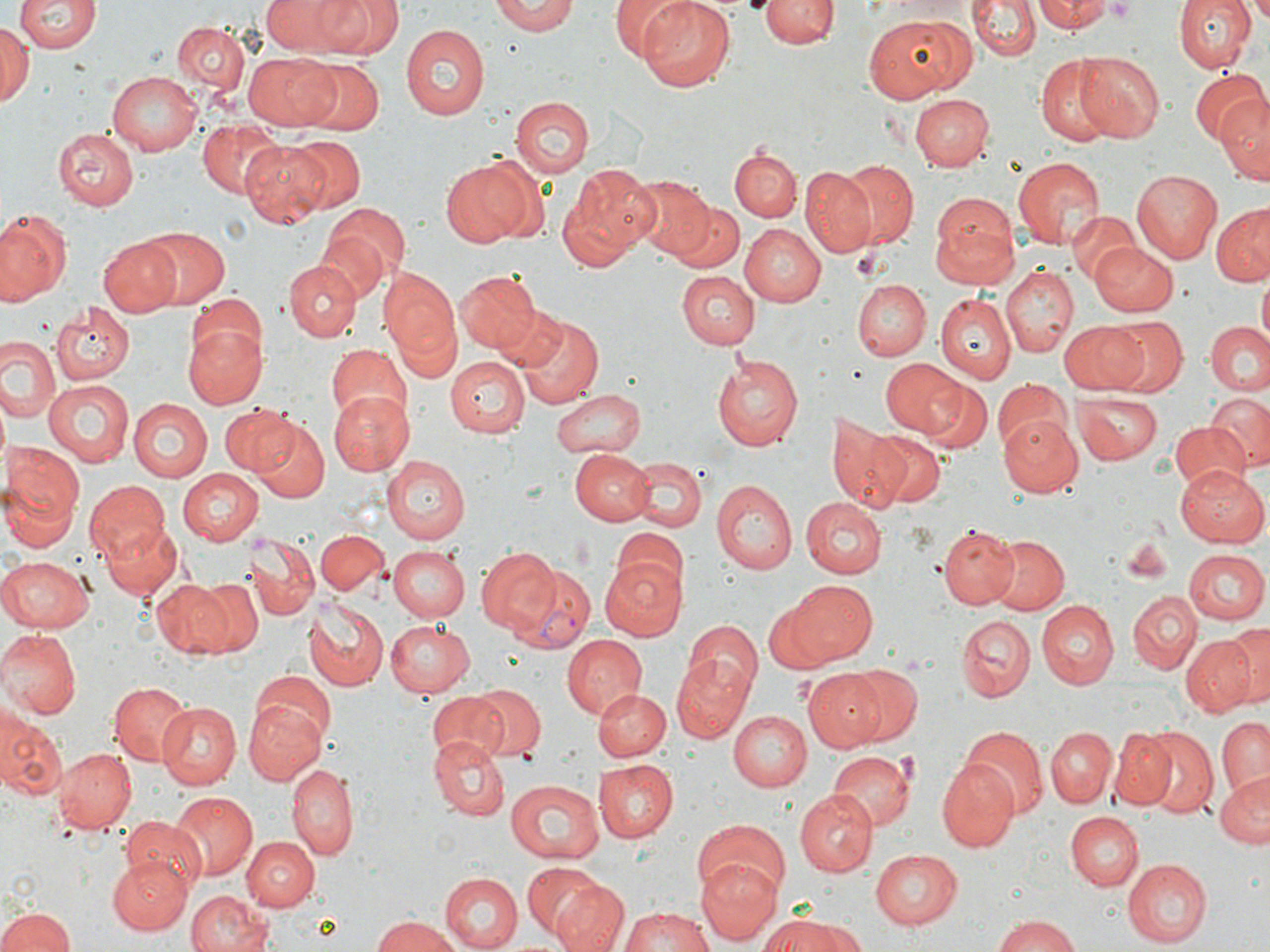

Summary:
  - Coordinate format: approximate bounding boxes as [x1, y1, x2, y2] in pixels
  - Plasmodium vivax-infected red blood cell locations: [513, 565, 594, 652]
  - Platelet locations: [1102, 0, 1141, 21]
  - Uninfected red blood cell locations: [263, 0, 356, 54], [318, 0, 400, 56], [493, 0, 578, 35], [614, 0, 698, 63], [638, 0, 736, 91], [760, 0, 835, 49], [969, 0, 1038, 62], [1037, 0, 1111, 33], [1173, 0, 1255, 74], [15, 1, 99, 56], [862, 14, 973, 100], [171, 20, 249, 100], [1, 23, 35, 107], [399, 24, 487, 121], [246, 51, 339, 130], [1075, 51, 1164, 138], [1035, 59, 1115, 143], [300, 60, 384, 136], [106, 69, 203, 154], [1189, 70, 1270, 145], [911, 93, 994, 169], [1215, 93, 1269, 180], [510, 96, 594, 178], [198, 119, 280, 198], [55, 125, 141, 208], [285, 135, 364, 212], [242, 139, 334, 225], [731, 147, 802, 223], [1009, 156, 1104, 249], [439, 158, 536, 248], [835, 160, 919, 248], [563, 165, 660, 258], [801, 168, 876, 258], [1131, 170, 1222, 263], [629, 177, 713, 260], [930, 197, 1020, 288], [673, 200, 743, 274], [319, 201, 408, 284], [1212, 204, 1270, 287], [0, 208, 72, 305], [1065, 210, 1143, 289], [740, 223, 826, 306], [138, 227, 229, 308], [318, 228, 389, 302], [99, 235, 183, 315], [1089, 241, 1179, 317], [285, 259, 360, 340], [999, 265, 1078, 357], [378, 268, 463, 373], [455, 269, 542, 354], [678, 270, 760, 349], [1257, 275, 1270, 340], [853, 280, 931, 359], [936, 293, 1017, 384], [193, 294, 266, 363], [491, 303, 572, 376], [51, 305, 133, 385], [516, 311, 605, 408], [1106, 317, 1189, 398], [183, 320, 265, 409], [1206, 320, 1270, 395], [1059, 322, 1150, 391], [0, 338, 62, 425], [326, 343, 411, 427], [710, 355, 803, 452], [444, 356, 527, 436], [879, 356, 963, 437], [994, 378, 1072, 457], [43, 379, 133, 467], [921, 379, 993, 455], [549, 387, 647, 458], [326, 391, 414, 474], [1072, 392, 1161, 468], [1207, 392, 1270, 470], [127, 399, 211, 480], [221, 402, 296, 475], [998, 413, 1084, 496], [821, 417, 908, 514], [253, 418, 330, 503], [1169, 419, 1248, 492], [869, 428, 945, 509], [570, 449, 654, 524], [0, 455, 83, 547], [381, 455, 468, 544], [631, 458, 707, 531], [1176, 465, 1269, 548], [177, 468, 264, 546], [84, 478, 169, 565], [713, 481, 795, 575], [800, 497, 887, 579], [101, 521, 182, 600], [938, 525, 1018, 609], [608, 531, 685, 606], [317, 532, 387, 593], [246, 535, 318, 618], [988, 535, 1069, 616], [389, 545, 470, 620], [475, 548, 561, 636], [1183, 549, 1268, 625], [0, 553, 93, 632], [598, 556, 686, 641], [151, 580, 231, 657], [189, 580, 262, 654], [786, 580, 878, 665], [1127, 590, 1202, 673], [302, 594, 388, 692], [765, 597, 841, 672], [1037, 600, 1119, 687], [956, 615, 1035, 702], [385, 618, 475, 697], [1229, 618, 1269, 710], [684, 621, 762, 704], [0, 629, 79, 720], [1180, 634, 1256, 717], [564, 635, 649, 719], [671, 658, 751, 742], [843, 666, 923, 746], [804, 669, 889, 750], [248, 673, 335, 746], [107, 681, 191, 766], [464, 683, 546, 761], [594, 689, 671, 761], [427, 690, 510, 765], [245, 699, 328, 783], [153, 700, 242, 790], [727, 710, 811, 790], [3, 715, 66, 801], [1215, 717, 1269, 802], [1046, 727, 1115, 807], [1137, 727, 1218, 816], [962, 728, 1047, 818], [1110, 729, 1177, 810], [430, 736, 509, 819], [53, 748, 136, 834], [828, 751, 916, 831], [936, 756, 1020, 853], [597, 757, 680, 842], [288, 764, 359, 860], [1215, 772, 1270, 850], [504, 779, 604, 864], [792, 789, 877, 878], [169, 792, 258, 882], [1065, 811, 1143, 890], [120, 816, 206, 891], [692, 817, 789, 904], [241, 836, 317, 912], [869, 848, 962, 928], [106, 856, 192, 936], [695, 856, 780, 942], [1123, 858, 1212, 945], [523, 862, 606, 938], [439, 873, 521, 950], [554, 881, 629, 952], [185, 889, 276, 952], [0, 903, 79, 952], [620, 907, 719, 952], [370, 915, 461, 952], [991, 915, 1086, 952], [765, 916, 858, 952]
  - Slide-level diagnosis: Plasmodium vivax
  - Magnification: 1000x
  - Field of view: one of a larger specimen
  - Preparation: thin blood film
  - Modality: optical microscopy
  - Image size: 1270×952 pixels
  - Stain: May-Grünwald-Giemsa